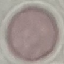

Malaria status: uninfected. Thin smear of blood. Giemsa stain. Cell patch, automatically extracted from a larger field of view and resized to 64 × 64 pixels. Acquired by smartphone through the microscope eyepiece.